Classify this cell by malaria status.
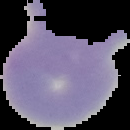
Uninfected.

Summary:
  - Image size: 130×130 pixels
  - Preparation: thin blood smear
  - Image type: segmented cell region with the area outside set to black